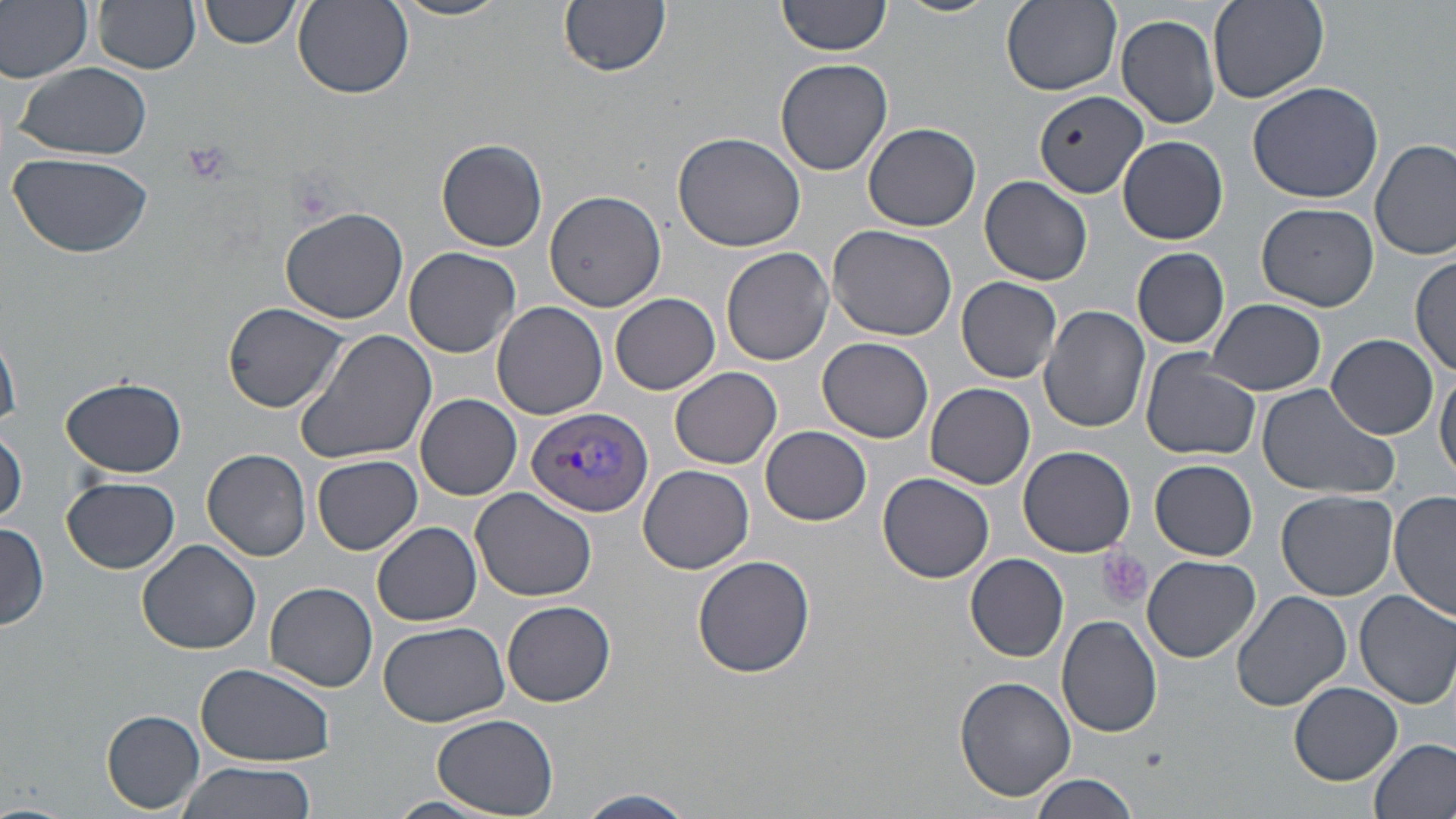

Approximate bounding boxes as [x1, y1, x2, y2] in pixels. Uninfected red blood cell locations: [0, 0, 95, 83], [94, 0, 201, 74], [201, 0, 301, 49], [778, 0, 893, 56], [889, 0, 998, 17], [391, 1, 513, 22], [558, 1, 670, 76], [1000, 1, 1121, 95], [1207, 1, 1329, 103], [293, 2, 414, 99], [1117, 13, 1223, 128], [774, 58, 893, 176], [11, 61, 151, 160], [1247, 79, 1387, 206], [1033, 91, 1146, 201], [863, 122, 981, 232], [671, 131, 806, 251], [1118, 135, 1228, 244], [437, 138, 548, 252], [1371, 138, 1455, 260], [7, 154, 152, 259], [980, 176, 1092, 285], [543, 190, 669, 313], [1256, 202, 1379, 311], [280, 206, 408, 323], [827, 225, 958, 342], [720, 245, 834, 367], [404, 247, 523, 359], [1132, 247, 1230, 348], [1411, 253, 1454, 376], [956, 276, 1063, 382], [609, 293, 721, 395], [1207, 298, 1328, 394], [223, 302, 349, 412], [492, 302, 609, 420], [1039, 305, 1150, 433], [298, 329, 441, 464], [1326, 333, 1439, 439], [0, 337, 21, 427], [818, 337, 934, 444], [1140, 351, 1260, 460], [669, 365, 782, 468], [1434, 367, 1456, 481], [62, 375, 186, 478], [925, 382, 1035, 490], [1255, 385, 1400, 500], [415, 393, 521, 499], [759, 424, 872, 526], [1, 429, 26, 524], [1018, 445, 1136, 557], [203, 448, 312, 561], [312, 454, 422, 555], [1150, 459, 1259, 561], [639, 465, 754, 573], [879, 472, 994, 582], [62, 476, 180, 574], [471, 489, 597, 602], [1277, 489, 1397, 602], [1390, 490, 1456, 621], [373, 522, 481, 626], [0, 524, 49, 632], [138, 540, 262, 655], [966, 553, 1069, 661], [693, 554, 815, 679], [1142, 555, 1260, 662], [266, 582, 378, 692], [1231, 590, 1352, 714], [1354, 590, 1456, 708], [502, 599, 617, 708], [1057, 614, 1165, 737], [379, 620, 510, 728], [196, 661, 334, 765], [954, 674, 1076, 804], [1289, 682, 1402, 784], [102, 710, 204, 813], [432, 713, 559, 816], [1370, 738, 1456, 819], [175, 760, 317, 819], [1028, 775, 1144, 819], [577, 788, 695, 819], [387, 795, 500, 818]. Plasmodium vivax-infected red blood cell locations: [526, 406, 654, 518]. Platelet locations: [179, 138, 233, 188], [1095, 549, 1153, 612]. Slide-level diagnosis: Plasmodium vivax. May-Grünwald-Giemsa stain. Captured at 1000x magnification. Optical microscopy. Thin blood smear. Single field of view. Image is 1456×819 pixels.